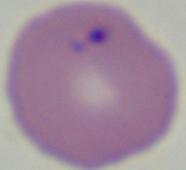

1000x magnification. A Babesia parasite is shown. Photomicrograph.